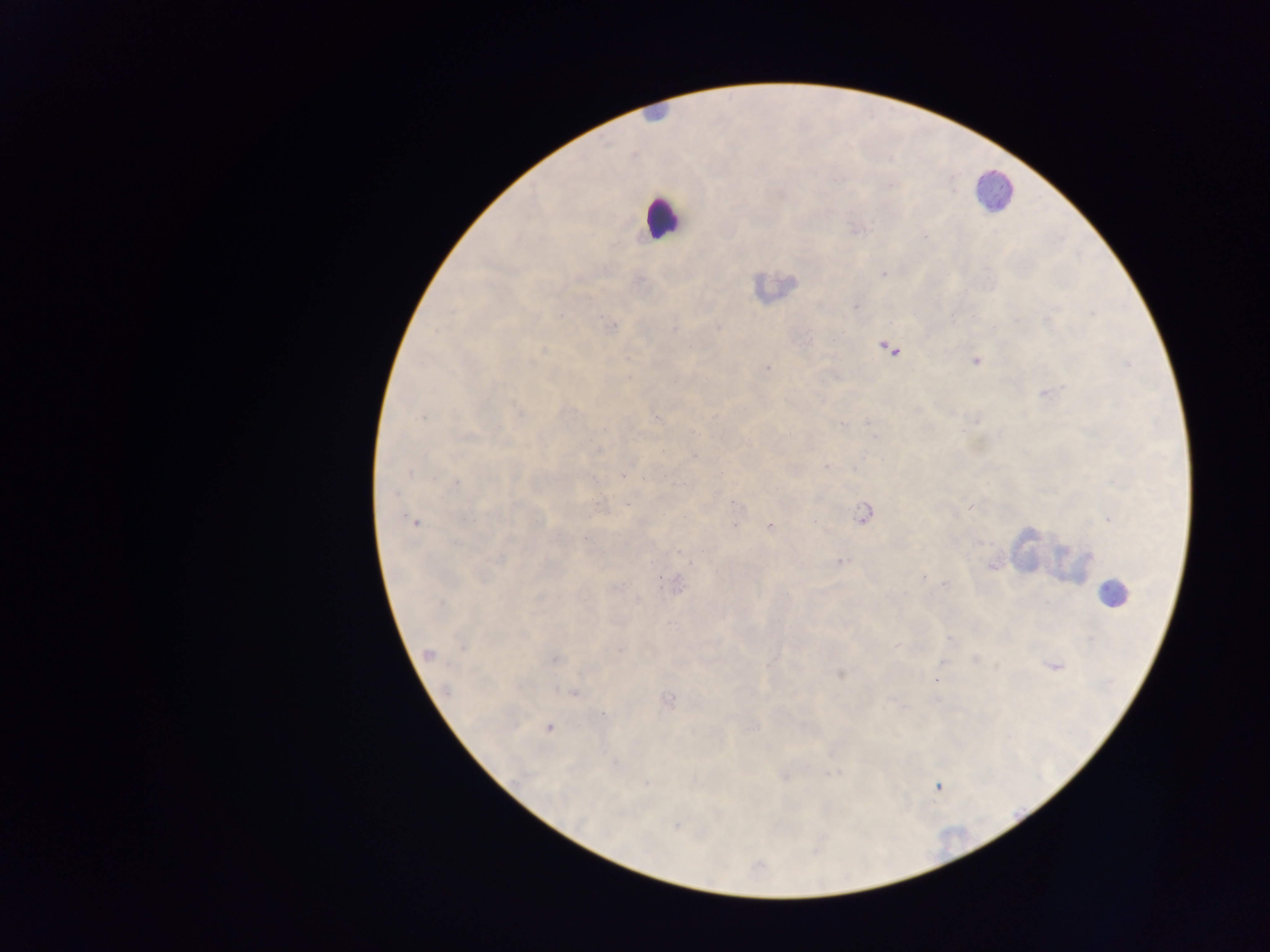
Approximate centers as (x, y) in pixels. Malaria parasite locations: (925, 236), (884, 274), (719, 326), (609, 327), (890, 349), (975, 360), (766, 368), (1045, 392), (518, 411), (869, 422), (597, 450), (694, 456), (827, 466), (625, 475), (453, 483), (601, 503), (736, 504), (864, 513), (1108, 518), (414, 522), (769, 525), (585, 536), (839, 561), (992, 564), (675, 583), (944, 583), (638, 600), (948, 639), (898, 646), (428, 655), (554, 659), (770, 662), (1054, 666), (839, 674), (572, 692), (667, 700), (548, 727), (832, 772), (783, 774), (938, 786), (678, 825). Leukocyte locations: (655, 114), (993, 192), (661, 217), (773, 289), (1044, 552), (1067, 562), (1113, 594). Image is 1270×952 pixels. Collected in Ghana. Thick blood film. One field of view. Mobile-phone photograph taken through the microscope.